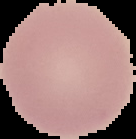

Image is 136×139 pixels. From a thin blood film. Malaria status: uninfected. The area outside the segmented cell region is set to black.